Outline each Plasmodium ovale-infected red blood cell.
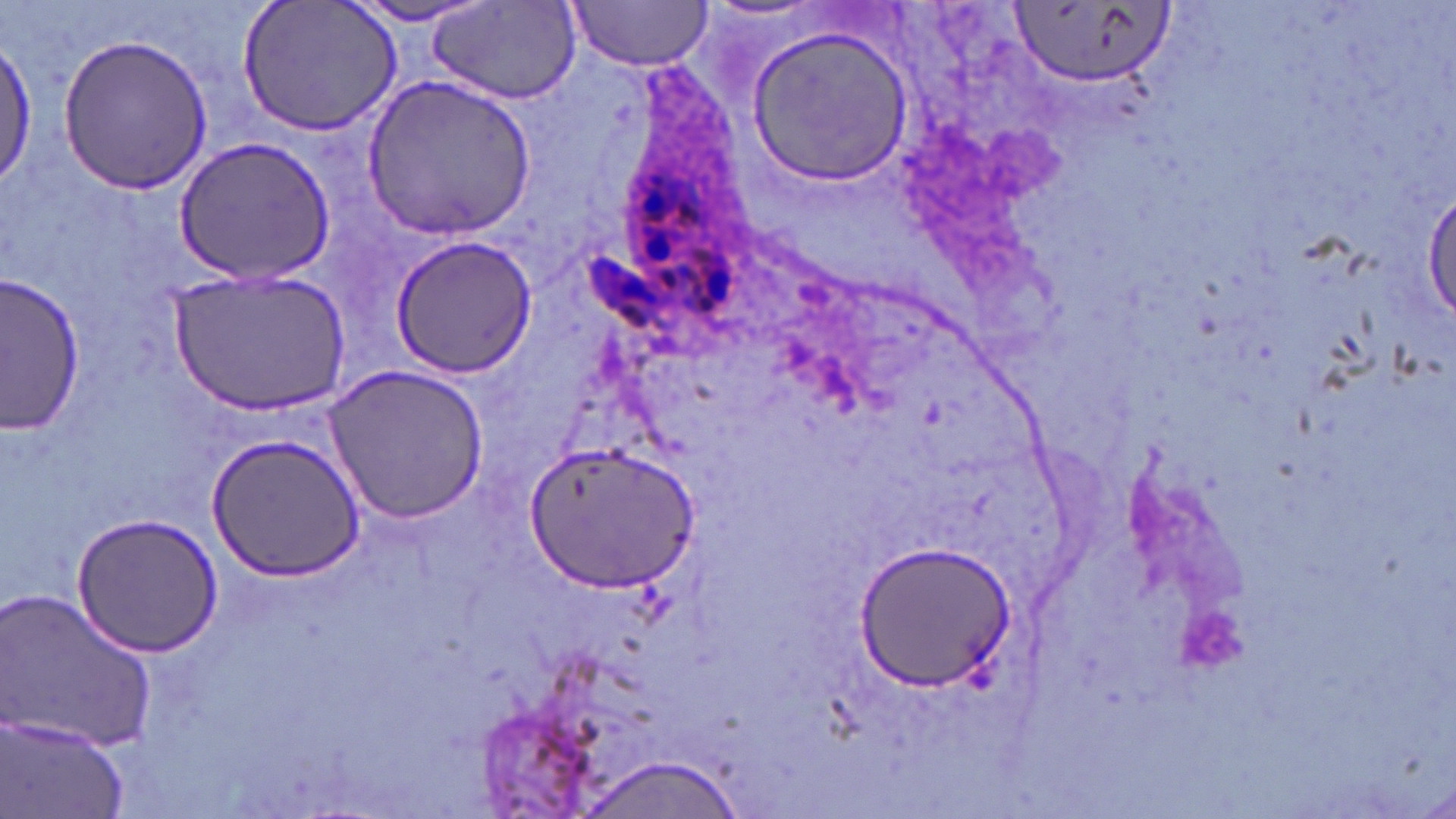

Approximate bounding boxes as (x1, y1, x2, y2) in pixels.
Plasmodium ovale-infected red blood cells: (572, 160, 761, 352).

slide-level diagnosis = Plasmodium ovale
preparation = thin blood film
magnification = 1000x
uninfected red blood cell locations = approximate bounding boxes as (x1, y1, x2, y2) in pixels: (566, 0, 714, 71), (238, 1, 402, 139), (429, 1, 582, 107), (1006, 1, 1175, 90), (344, 2, 494, 29), (748, 25, 916, 187), (53, 32, 216, 195), (0, 35, 37, 190), (364, 74, 537, 237), (173, 136, 337, 285), (1421, 181, 1454, 328), (389, 235, 537, 379), (165, 269, 354, 419), (3, 273, 85, 433), (326, 363, 489, 523), (208, 433, 366, 580), (526, 437, 697, 596), (72, 510, 225, 658), (855, 542, 1018, 692), (1, 587, 160, 755), (3, 716, 128, 819), (572, 755, 754, 818)
stain = May-Grünwald-Giemsa
image size = 1456×819 pixels
modality = light microscopy
field of view = single